Report the malaria status of this cell.
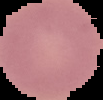
It is uninfected.

The area outside the segmented cell region is set to black. From a thin blood smear. Image is 103×100 pixels.